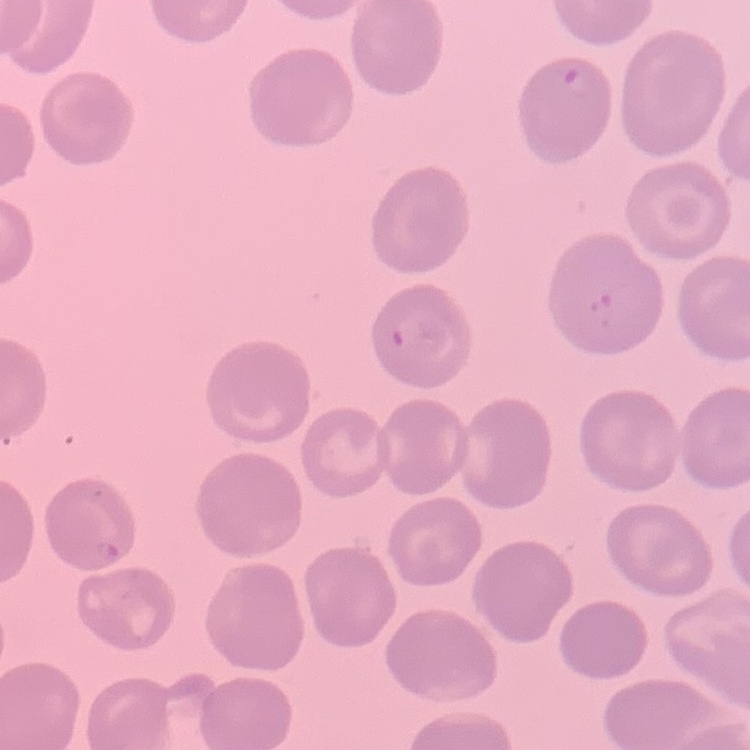
Summary:
  - Erythrocyte morphology: no rouleaux formation
  - Preparation: thin blood smear
  - Stain: Field's or Giemsa
  - Image type: one tile cut from a larger photomicrograph